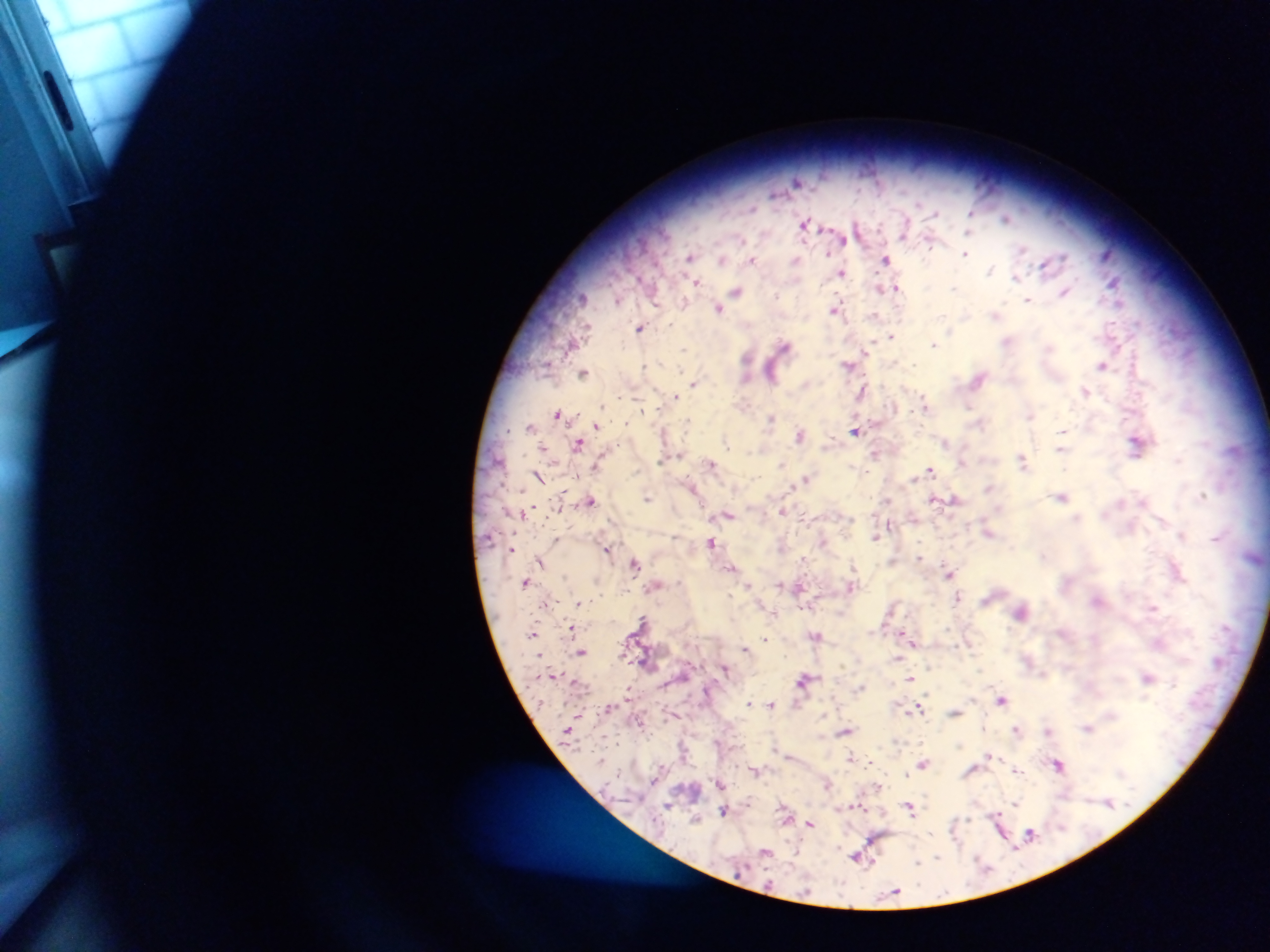

Approximate centers as {x, y} in pixels.
Summary:
  - Plasmodium parasite locations: {798, 182}, {972, 213}, {1007, 218}, {805, 225}, {840, 236}, {966, 254}, {1107, 254}, {690, 257}, {887, 258}, {723, 259}, {753, 260}, {796, 261}, {1047, 263}, {991, 270}, {842, 272}, {1017, 277}, {1114, 282}, {695, 283}, {890, 288}, {736, 291}, {1065, 291}, {582, 297}, {618, 300}, {1028, 300}, {725, 302}, {718, 307}, {837, 308}, {996, 314}, {641, 327}, {891, 336}, {1008, 341}, {934, 344}, {784, 345}, {685, 348}, {868, 350}, {749, 363}, {850, 365}, {1103, 365}, {646, 367}, {584, 371}, {772, 371}, {979, 378}, {694, 383}, {806, 384}, {1086, 390}, {863, 392}, {676, 396}, {926, 404}, {642, 409}, {558, 414}, {1031, 414}, {771, 417}, {980, 423}, {597, 424}, {531, 426}, {856, 430}, {801, 435}, {579, 442}, {946, 442}, {1138, 443}, {544, 447}, {1061, 448}, {875, 452}, {1023, 459}, {1178, 459}, {964, 461}, {712, 462}, {598, 463}, {782, 464}, {931, 471}, {538, 475}, {806, 479}, {693, 487}, {990, 487}, {1203, 494}, {1062, 496}, {647, 498}, {936, 499}, {590, 500}, {955, 500}, {1121, 502}, {560, 507}, {533, 509}, {783, 511}, {524, 512}, {728, 514}, {915, 517}, {1077, 518}, {890, 525}, {989, 531}, {876, 535}, {1182, 535}, {1217, 537}, {558, 539}, {823, 540}, {712, 543}, {512, 549}, {608, 549}, {1043, 556}, {919, 557}, {805, 558}, {892, 559}, {540, 561}, {636, 563}, {733, 567}, {1178, 569}, {949, 573}, {526, 581}, {781, 583}, {750, 584}, {657, 585}, {852, 586}, {799, 587}, {958, 595}, {1099, 600}, {578, 602}, {546, 604}, {1153, 607}, {891, 609}, {1021, 612}, {774, 614}, {644, 619}, {573, 628}, {534, 630}, {816, 636}, {766, 638}, {911, 640}, {746, 648}, {582, 652}, {898, 657}, {725, 670}, {1148, 677}, {910, 678}, {806, 679}, {861, 686}, {630, 688}, {1002, 699}, {751, 702}, {772, 704}, {609, 707}, {919, 707}, {955, 711}, {641, 721}, {1088, 727}, {1017, 729}, {845, 730}, {1050, 730}, {990, 755}, {851, 757}, {871, 761}, {924, 763}, {662, 765}, {1059, 765}, {756, 770}, {1017, 770}, {656, 781}, {720, 783}, {827, 783}, {878, 786}, {1109, 803}, {1016, 804}, {670, 805}, {859, 806}, {910, 806}, {724, 809}, {695, 819}, {810, 824}, {1001, 829}, {1031, 833}, {859, 856}, {938, 857}, {919, 862}, {894, 893}
  - Preparation: thick blood smear
  - Field of view: single
  - Image size: 1270×952 pixels
  - Capture: mobile-phone photograph through a microscope
  - Country: Ghana